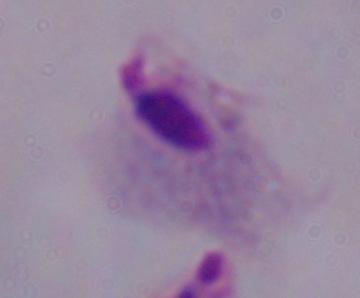

identification: trichomonad
modality: micrograph
magnification: 1000x